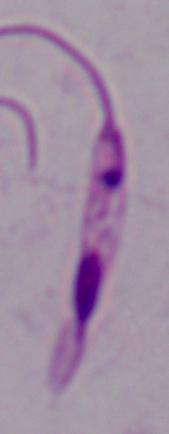
1000x magnification. A Leishmania parasite is shown. Photomicrograph.